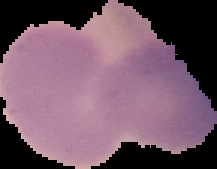

Summary:
  - Preparation: thin blood film
  - Malaria status: uninfected
  - Image type: cell region segmented out of the field of view; surrounding area masked to black
  - Image size: 217×169 pixels